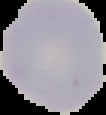

image_type: cell region segmented out of the field of view; surrounding area masked to black
preparation: thin blood smear
image_size: 106×115 pixels
malaria_status: uninfected